Name the parasite shown.
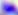

Toxoplasma gondii.

Captured at 400x magnification. Micrograph.